State which parasite is depicted.
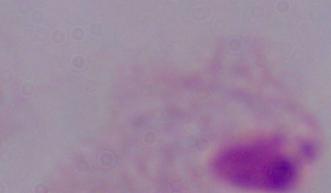

This is a trichomonad.

Micrograph. 1000x magnification.